Report the malaria status of this cell.
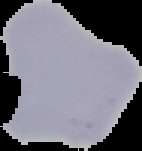

It is uninfected.

Image is 142×151 pixels. From a thin blood smear. Cell region segmented out of the field of view; the surrounding area is masked to black.